Locate and identify every blood parasite.
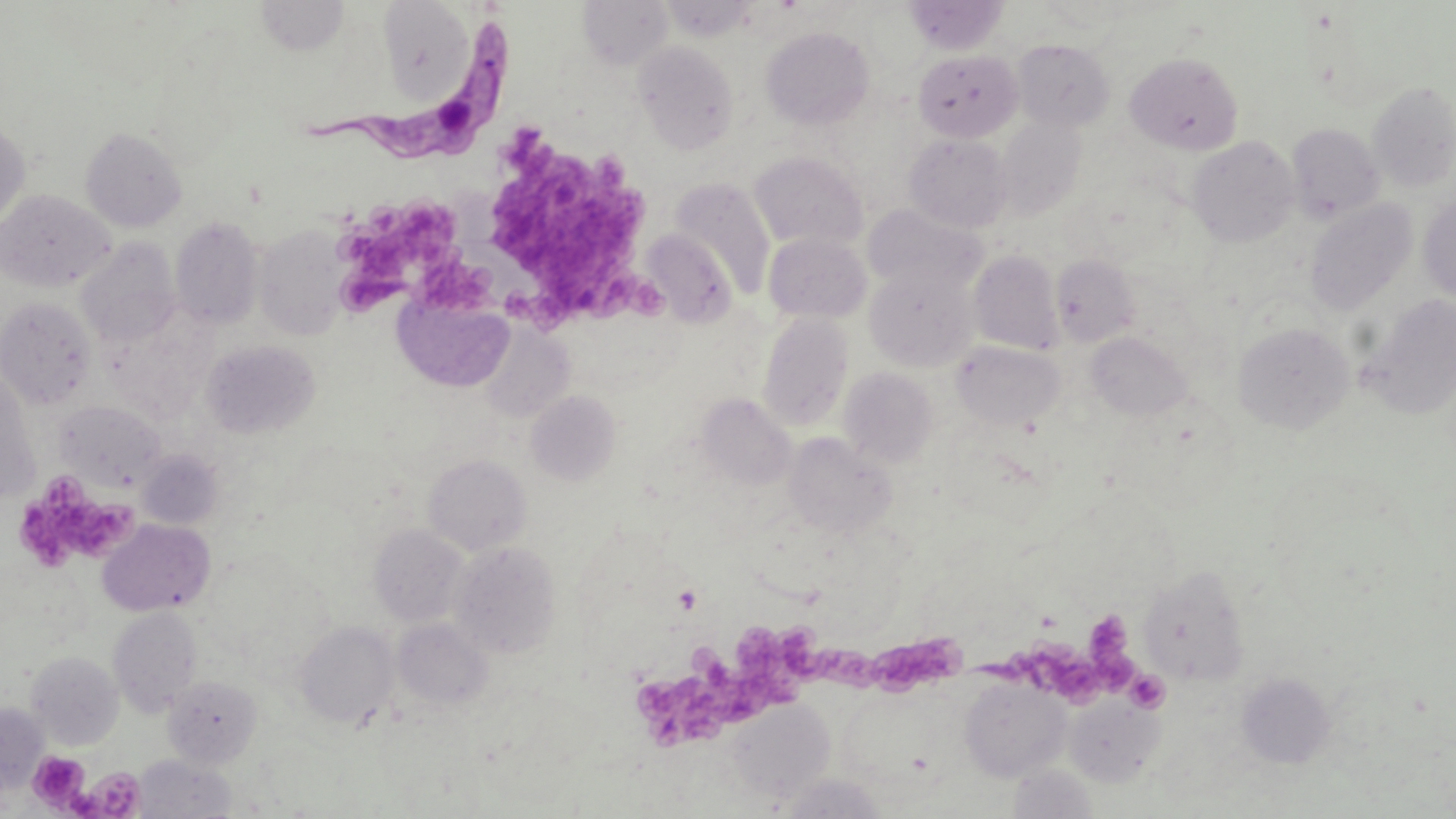
Approximate bounding boxes as (x1, y1, x2, y2) in pixels.
Trypanosoma brucei: (303, 18, 515, 161).
No Plasmodium falciparum, Plasmodium ovale, Plasmodium malariae, Plasmodium vivax, or Babesia divergens observed.

Summary:
  - Platelet locations: (488, 129, 662, 329), (373, 202, 468, 261), (362, 231, 422, 282), (410, 251, 513, 318), (342, 265, 402, 310), (19, 478, 142, 564), (673, 585, 703, 613), (1087, 611, 1133, 660), (635, 627, 816, 751), (807, 633, 883, 695), (870, 633, 972, 698), (988, 636, 1141, 707), (1127, 670, 1171, 713), (26, 751, 90, 811), (85, 766, 145, 817)
  - Uninfected red blood cell locations: (254, 0, 352, 56), (377, 0, 477, 101), (578, 0, 673, 69), (905, 0, 1007, 55), (761, 26, 875, 130), (1011, 38, 1115, 131), (634, 41, 739, 154), (913, 49, 1023, 142), (1126, 52, 1243, 155), (1367, 81, 1456, 192), (997, 117, 1086, 219), (0, 121, 30, 229), (1287, 123, 1384, 223), (81, 127, 186, 231), (904, 134, 1014, 232), (1189, 136, 1300, 247), (749, 151, 868, 252), (670, 178, 776, 298), (0, 189, 114, 291), (1419, 193, 1456, 302), (1304, 199, 1417, 315), (864, 205, 985, 295), (170, 217, 265, 329), (254, 226, 349, 341), (639, 230, 736, 326), (763, 232, 872, 323), (75, 238, 181, 348), (969, 250, 1063, 355), (1051, 254, 1140, 347), (866, 265, 977, 370), (392, 292, 514, 393), (1361, 295, 1456, 419), (0, 297, 97, 410), (758, 311, 854, 432), (1233, 321, 1355, 433), (479, 326, 574, 421), (1087, 332, 1192, 421), (201, 340, 321, 439), (952, 341, 1066, 431), (0, 367, 41, 503), (838, 367, 938, 468), (526, 390, 621, 486), (696, 393, 797, 488), (56, 400, 168, 492), (784, 433, 895, 538), (136, 449, 223, 530), (423, 453, 531, 555), (98, 519, 215, 616), (369, 523, 469, 627), (449, 541, 562, 659), (1138, 566, 1249, 685), (109, 606, 202, 717), (392, 618, 493, 711), (294, 620, 398, 729), (27, 651, 123, 750), (1237, 673, 1336, 768), (163, 675, 263, 769), (959, 677, 1071, 781), (839, 691, 935, 781), (1065, 695, 1163, 786), (725, 700, 835, 803), (0, 703, 47, 791), (133, 754, 236, 818), (1008, 764, 1097, 819)
  - Slide-level diagnosis: Trypanosoma brucei
  - Modality: optical microscopy
  - Preparation: thin blood smear
  - Image size: 1456×819 pixels
  - Stain: May-Grünwald-Giemsa
  - Field of view: single
  - Magnification: 1000x